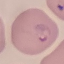

result = malaria parasites identified
capture = smartphone through the microscope eyepiece
stain = Giemsa
preparation = thin blood smear
image type = cell patch, automatically extracted from a larger field of view and resized to 64 × 64 pixels